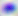
Captured at 400x magnification. Micrograph. Toxoplasma gondii is seen.